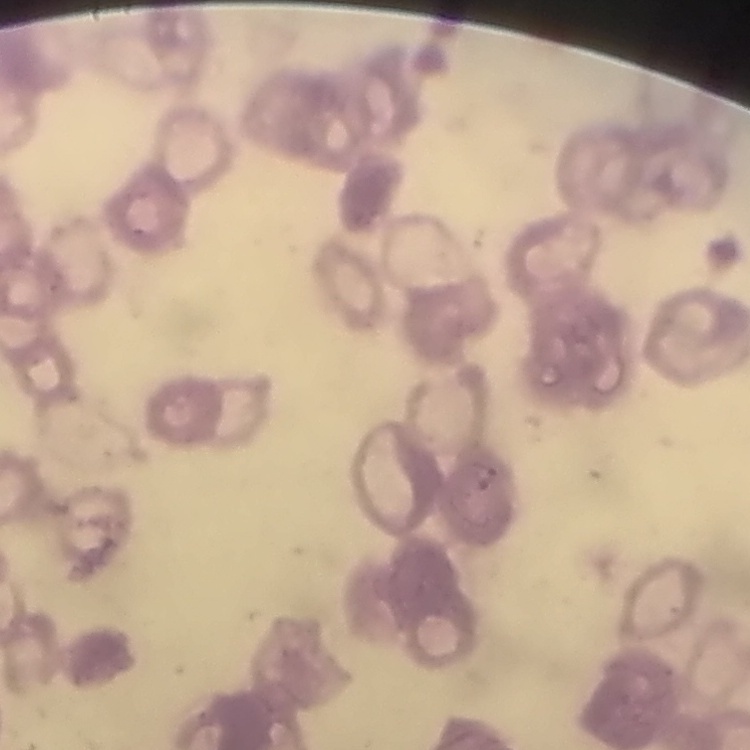

The red blood cells exhibit rouleaux formation. One tile cut from a larger photomicrograph. Thin blood film. Field's or Giemsa stain.